Identify the blood parasite species.
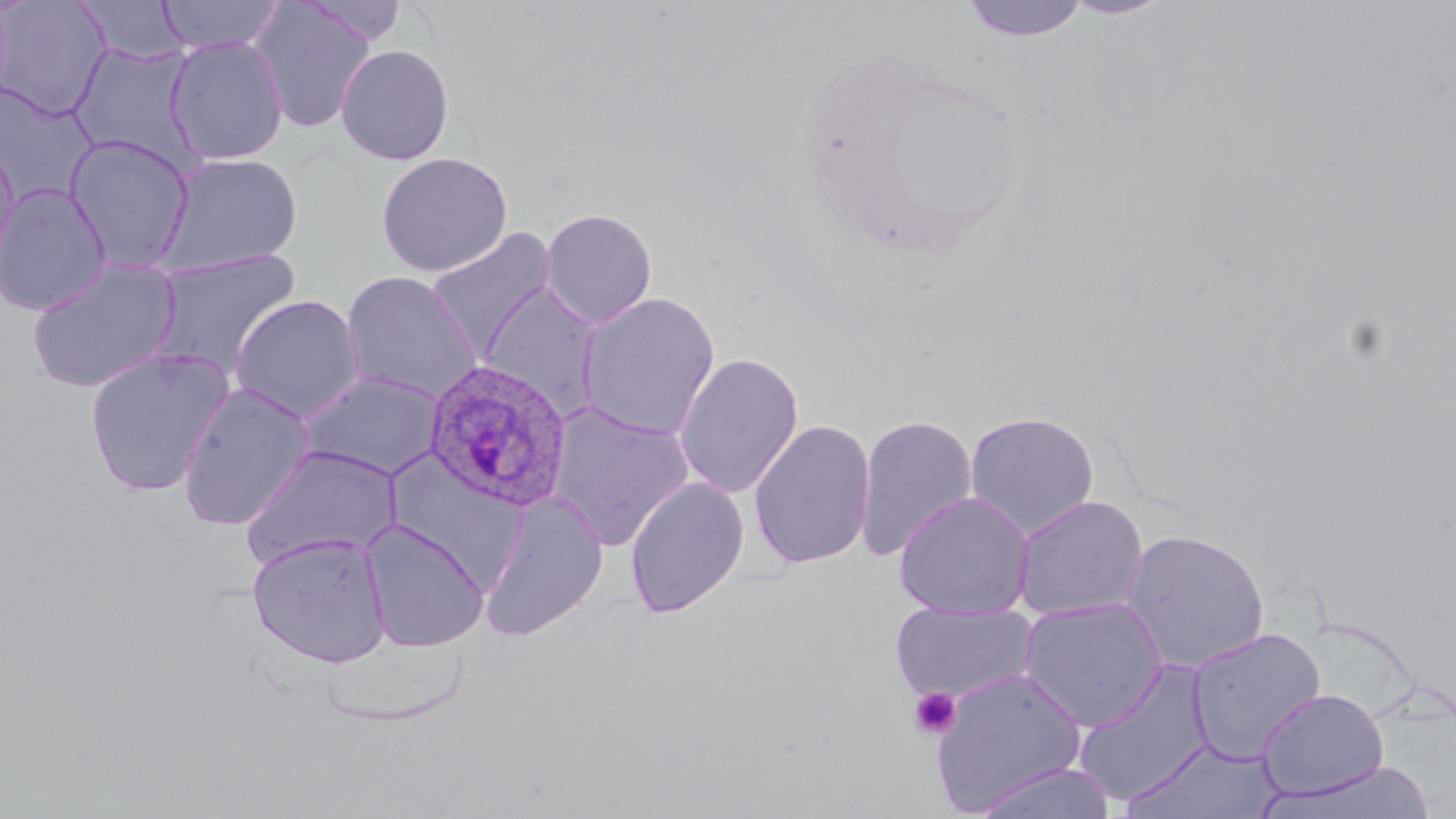
Plasmodium ovale.

Approximate bounding boxes as named x1/y1/x2/y2 corners in pixels. Uninfected red blood cell locations: (x1=155, y1=0, x2=287, y2=54), (x1=247, y1=0, x2=377, y2=132), (x1=299, y1=0, x2=412, y2=46), (x1=958, y1=0, x2=1092, y2=43), (x1=1059, y1=0, x2=1174, y2=20), (x1=0, y1=1, x2=112, y2=121), (x1=75, y1=1, x2=193, y2=66), (x1=165, y1=36, x2=289, y2=165), (x1=68, y1=41, x2=203, y2=172), (x1=335, y1=43, x2=455, y2=165), (x1=0, y1=84, x2=99, y2=205), (x1=63, y1=133, x2=196, y2=273), (x1=0, y1=140, x2=20, y2=279), (x1=154, y1=151, x2=303, y2=277), (x1=375, y1=151, x2=513, y2=277), (x1=0, y1=183, x2=111, y2=317), (x1=539, y1=207, x2=658, y2=330), (x1=425, y1=226, x2=559, y2=363), (x1=148, y1=249, x2=303, y2=381), (x1=26, y1=258, x2=181, y2=393), (x1=341, y1=270, x2=484, y2=404), (x1=476, y1=281, x2=605, y2=420), (x1=576, y1=291, x2=722, y2=441), (x1=230, y1=294, x2=366, y2=423), (x1=84, y1=347, x2=237, y2=498), (x1=674, y1=351, x2=804, y2=499), (x1=297, y1=370, x2=448, y2=481), (x1=176, y1=381, x2=314, y2=531), (x1=547, y1=401, x2=697, y2=551), (x1=965, y1=410, x2=1100, y2=538), (x1=854, y1=412, x2=979, y2=562), (x1=748, y1=418, x2=877, y2=570), (x1=241, y1=444, x2=403, y2=570), (x1=382, y1=450, x2=530, y2=590), (x1=624, y1=477, x2=750, y2=619), (x1=477, y1=490, x2=610, y2=642), (x1=894, y1=491, x2=1035, y2=619), (x1=1011, y1=495, x2=1149, y2=622), (x1=359, y1=520, x2=490, y2=652), (x1=1120, y1=528, x2=1271, y2=674), (x1=247, y1=533, x2=393, y2=668), (x1=1019, y1=597, x2=1168, y2=731), (x1=889, y1=602, x2=1039, y2=705), (x1=1186, y1=627, x2=1327, y2=763), (x1=1073, y1=659, x2=1215, y2=808), (x1=929, y1=667, x2=1086, y2=812), (x1=1257, y1=688, x2=1389, y2=799), (x1=1123, y1=738, x2=1284, y2=819), (x1=1266, y1=761, x2=1437, y2=819), (x1=967, y1=762, x2=1119, y2=819). Plasmodium ovale-infected red blood cell locations: (x1=422, y1=359, x2=574, y2=512). Platelet locations: (x1=909, y1=687, x2=962, y2=740). Light microscopy. One field of a larger specimen. Captured at 1000x magnification. Thin blood film. May-Grünwald-Giemsa-stained preparation. Image is 1456×819 pixels.